Locate every Plasmodium malariae-infected red blood cell.
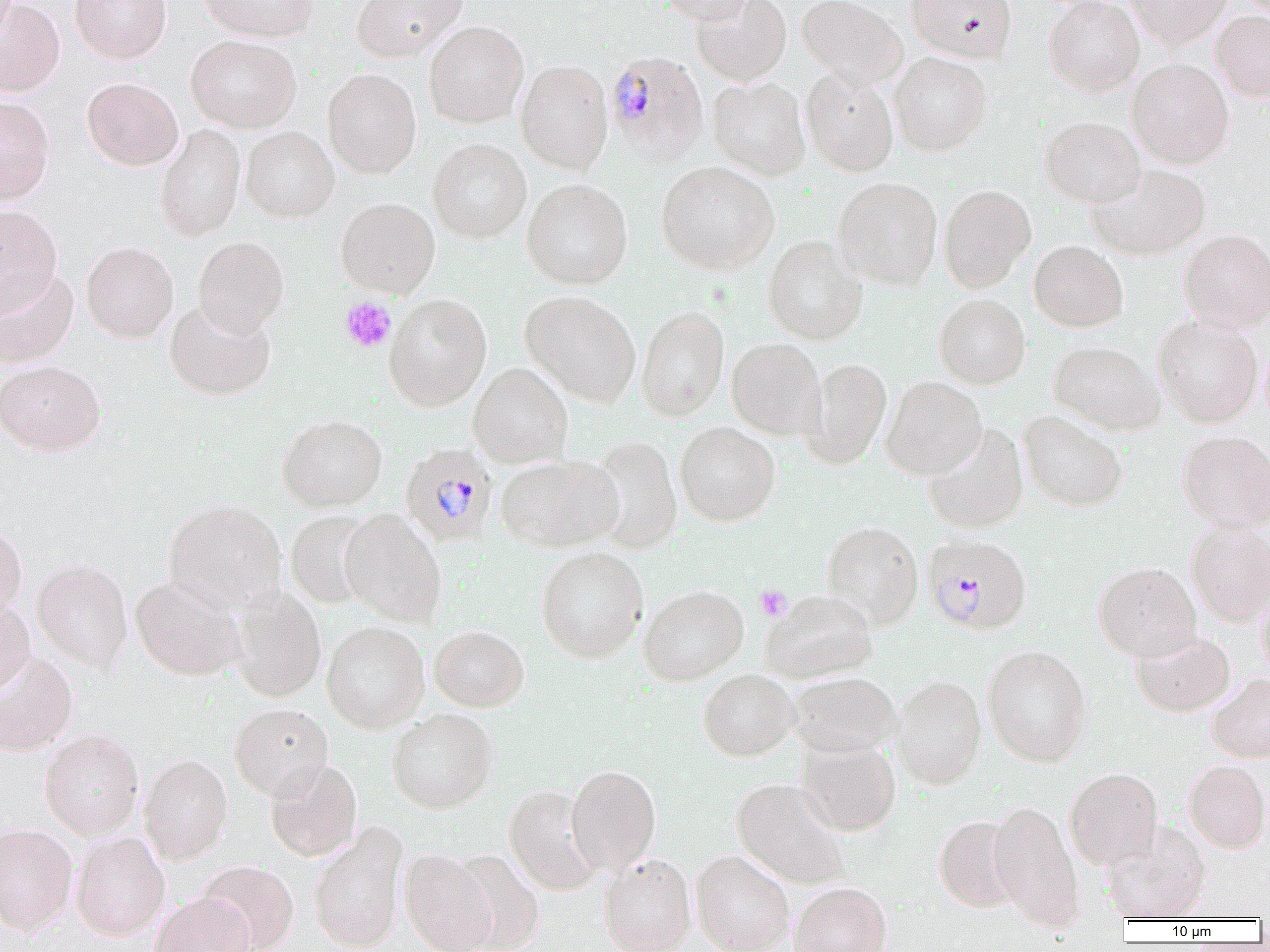
Approximate bounding boxes as [x1, y1, x2, y2] in pixels.
Plasmodium malariae-infected red blood cells: [605, 50, 709, 163], [400, 442, 498, 546], [922, 534, 1032, 634].

{
  "slide_level_diagnosis": "Plasmodium malariae",
  "field_of_view": "single",
  "modality": "light microscopy",
  "uninfected_red_blood_cell_locations": "approximate bounding boxes as [x1, y1, x2, y2] in pixels: [0, 0, 65, 97], [70, 0, 171, 63], [198, 0, 318, 42], [352, 0, 468, 61], [660, 0, 756, 24], [691, 0, 791, 85], [797, 0, 907, 88], [906, 0, 1016, 62], [1044, 0, 1144, 96], [1125, 0, 1231, 48], [1211, 11, 1270, 102], [423, 20, 529, 128], [186, 34, 302, 133], [889, 52, 992, 156], [1127, 58, 1235, 168], [515, 59, 613, 173], [323, 68, 421, 178], [800, 68, 899, 177], [82, 77, 183, 170], [707, 77, 811, 181], [0, 96, 55, 204], [1039, 116, 1146, 207], [155, 124, 246, 241], [241, 126, 339, 222], [428, 138, 531, 243], [656, 160, 779, 275], [1088, 164, 1211, 260], [833, 176, 943, 290], [522, 178, 633, 289], [939, 184, 1036, 293], [336, 197, 440, 298], [0, 205, 62, 315], [1178, 228, 1270, 334], [763, 235, 867, 345], [193, 236, 289, 336], [81, 241, 179, 343], [1029, 241, 1128, 331], [0, 267, 79, 368], [520, 291, 642, 407], [384, 294, 492, 411], [934, 294, 1030, 389], [165, 299, 276, 399], [637, 305, 729, 421], [1153, 316, 1262, 427], [727, 338, 826, 440], [1049, 340, 1165, 436], [802, 357, 893, 468], [0, 360, 105, 455], [469, 362, 573, 469], [881, 376, 986, 479], [1019, 409, 1128, 512], [277, 414, 388, 512], [674, 422, 780, 526], [923, 422, 1028, 534], [1177, 430, 1270, 532], [587, 435, 683, 554], [495, 454, 622, 552], [163, 498, 288, 614], [340, 509, 447, 627], [286, 510, 379, 609], [822, 520, 923, 630], [1186, 520, 1270, 628], [0, 524, 28, 619], [536, 546, 649, 663], [32, 558, 133, 673], [1094, 561, 1202, 662], [130, 576, 247, 681], [638, 585, 748, 685], [229, 586, 327, 702], [1257, 588, 1270, 680], [761, 589, 878, 683], [0, 593, 36, 694], [321, 621, 429, 733], [429, 625, 529, 711], [1131, 627, 1236, 716], [982, 645, 1092, 767], [0, 651, 77, 756], [698, 668, 799, 761], [788, 672, 901, 757], [1207, 673, 1270, 762], [890, 674, 987, 790], [229, 703, 333, 800], [387, 708, 498, 813], [40, 728, 144, 839], [797, 737, 901, 836], [138, 753, 233, 864], [265, 759, 362, 861], [1184, 760, 1270, 853], [566, 764, 661, 876], [1064, 767, 1163, 870], [731, 778, 852, 890], [504, 784, 604, 895], [988, 800, 1083, 930], [934, 815, 1022, 913], [308, 821, 408, 952], [1103, 821, 1212, 922], [0, 823, 78, 935], [71, 831, 170, 941], [400, 848, 497, 952], [449, 849, 545, 952], [691, 849, 795, 952], [598, 853, 697, 952], [196, 859, 299, 952], [789, 881, 891, 952], [150, 892, 254, 952]",
  "magnification": "1000x",
  "preparation": "thin blood smear",
  "platelet_locations": "approximate bounding boxes as [x1, y1, x2, y2] in pixels: [340, 296, 396, 353], [755, 585, 792, 621]",
  "image_size": "1270×952 pixels"
}